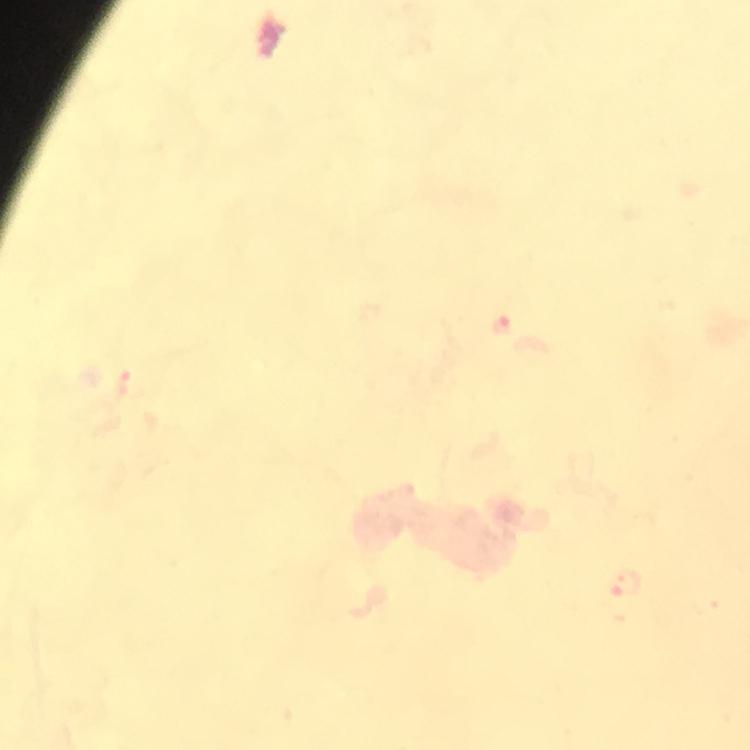

Approximate centers as [x, y] in pixels.
Summary:
  - Malaria parasite locations: [503, 322], [626, 582]
  - Magnification: 100x
  - Preparation: thick smear
  - Image size: 750×750 pixels
  - Cropped from: a single field of view
  - Context: from a diagnostic examination for malaria
  - Stain: Giemsa
  - Immersion oil: applied
  - Capture: smartphone mounted on the microscope